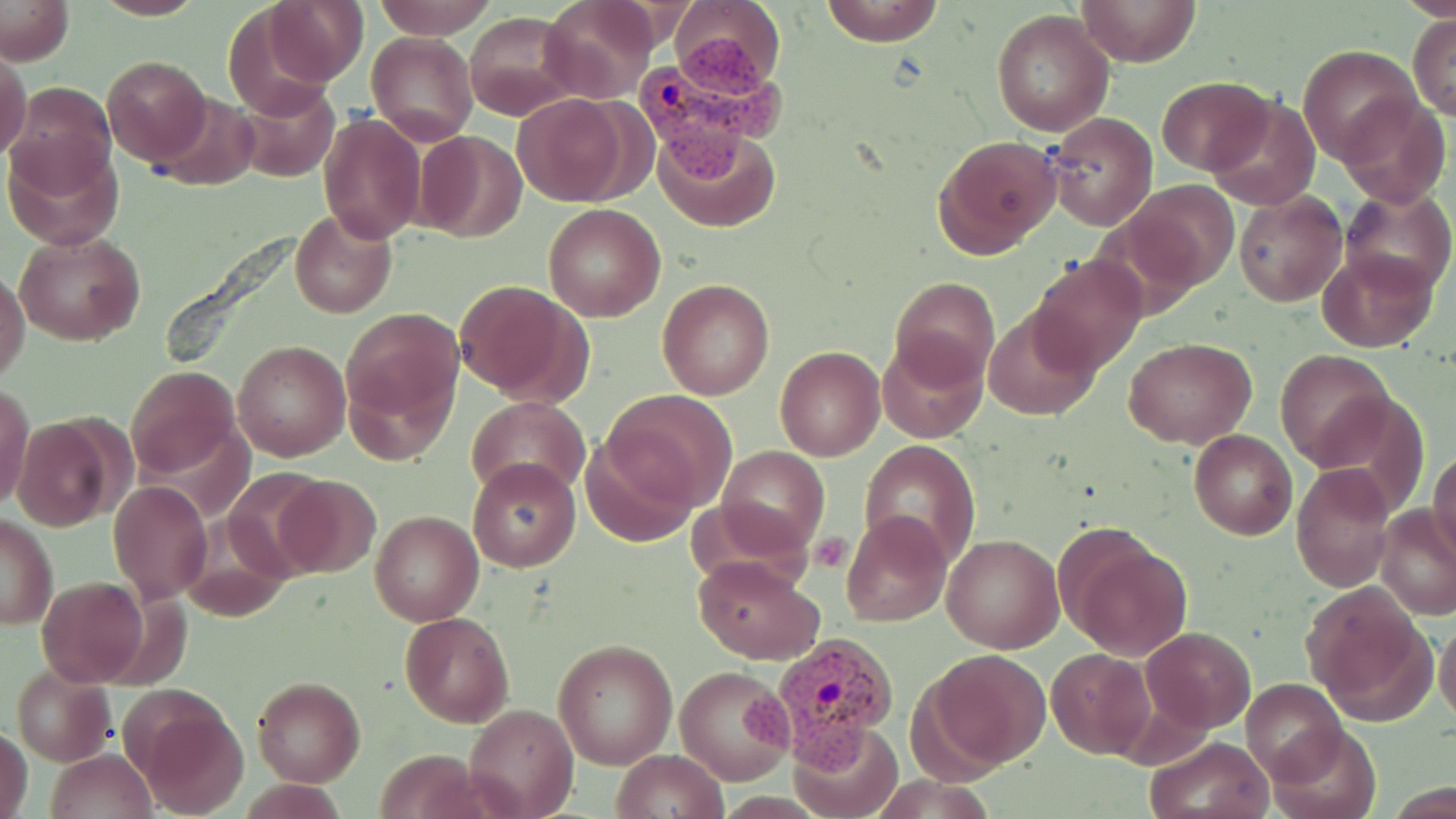

Summary:
  - Coordinate format: approximate bounding boxes as [x1, y1, x2, y2] in pixels
  - Uninfected red blood cell locations: [91, 0, 206, 19], [371, 0, 499, 39], [819, 0, 947, 47], [1075, 0, 1202, 68], [1, 1, 74, 64], [263, 1, 369, 86], [538, 1, 656, 103], [221, 3, 348, 117], [666, 4, 785, 95], [990, 8, 1115, 137], [464, 13, 581, 120], [1408, 15, 1455, 119], [366, 31, 478, 144], [1299, 45, 1419, 161], [0, 46, 32, 164], [100, 54, 212, 167], [1157, 76, 1271, 173], [9, 81, 117, 195], [234, 81, 340, 183], [149, 92, 259, 192], [512, 93, 636, 206], [1204, 94, 1322, 212], [1337, 94, 1449, 206], [317, 112, 425, 244], [1044, 112, 1158, 230], [652, 126, 780, 233], [413, 131, 527, 242], [932, 134, 1062, 258], [4, 140, 124, 248], [1130, 178, 1238, 288], [1339, 185, 1454, 299], [1235, 192, 1346, 306], [542, 204, 666, 321], [290, 209, 395, 317], [13, 229, 146, 346], [1316, 247, 1439, 352], [1028, 255, 1148, 375], [0, 266, 29, 386], [890, 276, 1000, 387], [658, 278, 775, 401], [453, 279, 587, 402], [983, 306, 1101, 421], [342, 308, 464, 453], [877, 336, 988, 443], [1123, 336, 1257, 448], [233, 339, 350, 462], [775, 346, 884, 460], [1274, 349, 1394, 468], [124, 365, 240, 482], [2, 385, 35, 513], [605, 390, 736, 509], [468, 399, 588, 498], [10, 416, 120, 532], [1189, 429, 1297, 540], [582, 430, 697, 548], [859, 439, 981, 565], [717, 446, 829, 556], [1430, 446, 1456, 561], [468, 458, 579, 571], [1291, 463, 1396, 592], [272, 473, 383, 579], [108, 480, 212, 603], [688, 495, 817, 597], [1375, 505, 1455, 620], [181, 509, 293, 621], [370, 510, 482, 624], [842, 510, 950, 627], [1, 515, 58, 629], [943, 534, 1063, 652], [1066, 534, 1192, 660], [691, 557, 823, 664], [38, 576, 150, 687], [1302, 586, 1432, 724], [400, 611, 516, 727], [1435, 618, 1456, 725], [1141, 626, 1256, 733], [553, 638, 677, 769], [923, 648, 1052, 770], [1045, 648, 1156, 759], [9, 665, 115, 767], [675, 665, 793, 785], [252, 677, 364, 786], [1243, 678, 1348, 785], [133, 693, 251, 817], [465, 702, 578, 818], [791, 720, 901, 818], [1266, 722, 1382, 819], [1, 727, 33, 819], [1145, 735, 1273, 818], [611, 748, 728, 819], [46, 749, 154, 819]
  - Plasmodium vivax-infected red blood cell locations: [634, 34, 782, 178], [738, 632, 899, 777]
  - Platelet locations: [810, 531, 851, 572]
  - Slide-level diagnosis: Plasmodium vivax
  - Magnification: 1000x
  - Preparation: thin blood film
  - Modality: light microscopy
  - Field of view: one of a larger specimen
  - Image size: 1456×819 pixels
  - Stain: May-Grünwald-Giemsa